Identify the parasite.
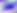

This is Toxoplasma gondii.

Micrograph. 400x magnification.